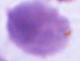
Captured at 1000x magnification. A red blood cell is seen. Photomicrograph.